Classify this cell by malaria status.
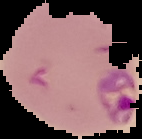

Parasitized.

image size = 142×139 pixels
image type = segmented cell region on a black background
preparation = thin blood film